Outline each blood parasite and name the species.
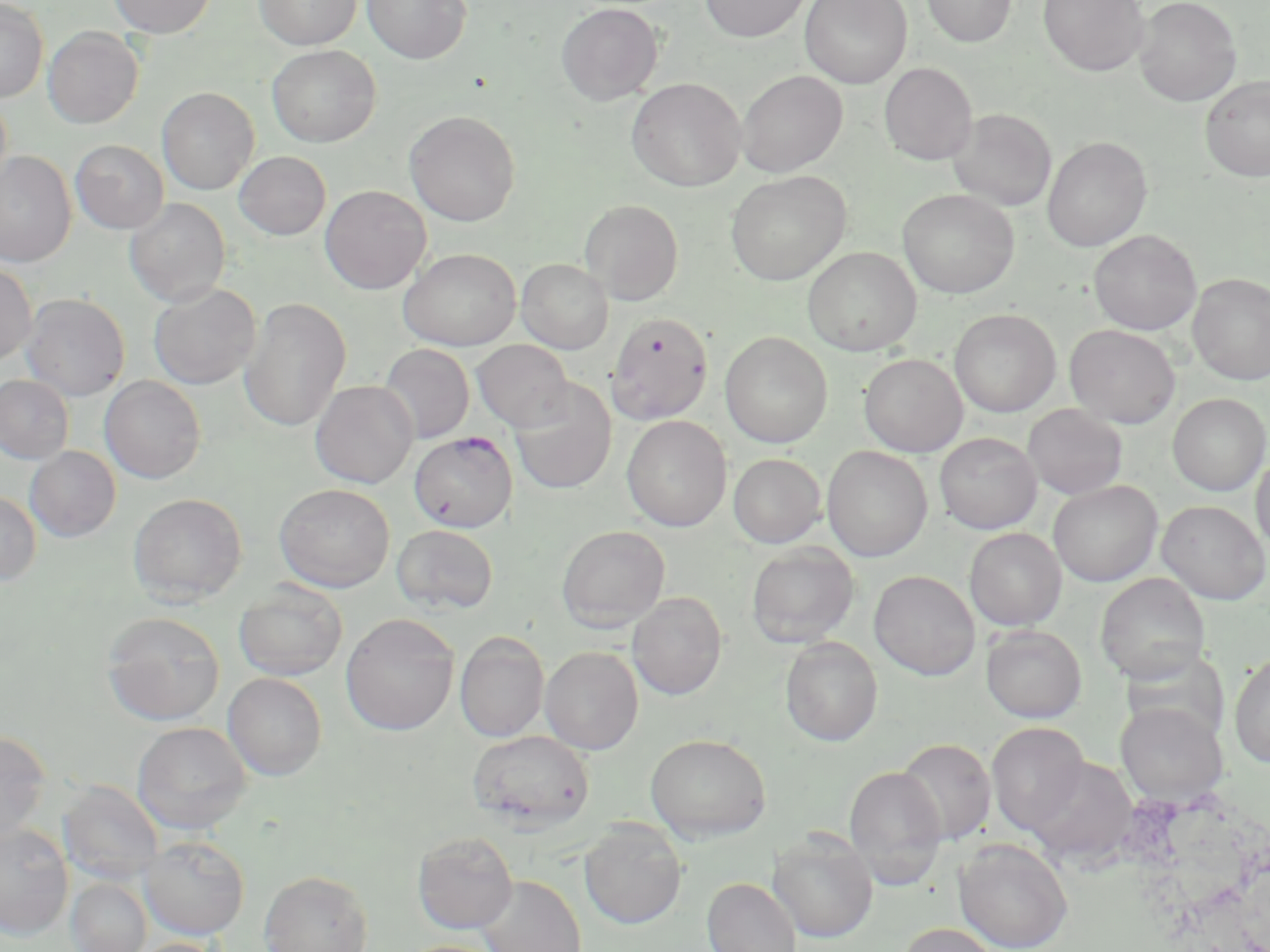

Approximate bounding boxes as named x1/y1/x2/y2 corners in pixels.
Plasmodium falciparum-infected red blood cells: (x1=409, y1=431, x2=518, y2=532).
No Plasmodium ovale, Plasmodium malariae, Plasmodium vivax, Babesia divergens, or Trypanosoma brucei observed.

{
  "slide_level_diagnosis": "Plasmodium falciparum",
  "modality": "light microscopy",
  "image_size": "1270×952 pixels",
  "stain": "May-Grünwald-Giemsa",
  "field_of_view": "single",
  "uninfected_red_blood_cell_locations": "approximate bounding boxes as named x1/y1/x2/y2 corners in pixels: (x1=109, y1=0, x2=216, y2=37), (x1=254, y1=0, x2=361, y2=50), (x1=363, y1=0, x2=471, y2=64), (x1=699, y1=0, x2=812, y2=42), (x1=800, y1=0, x2=911, y2=88), (x1=921, y1=0, x2=1016, y2=47), (x1=1038, y1=0, x2=1149, y2=77), (x1=1134, y1=0, x2=1242, y2=106), (x1=0, y1=1, x2=48, y2=102), (x1=555, y1=2, x2=663, y2=105), (x1=43, y1=26, x2=143, y2=128), (x1=267, y1=45, x2=381, y2=147), (x1=879, y1=62, x2=978, y2=165), (x1=737, y1=70, x2=848, y2=177), (x1=1200, y1=75, x2=1270, y2=182), (x1=626, y1=77, x2=746, y2=192), (x1=157, y1=87, x2=259, y2=195), (x1=0, y1=92, x2=12, y2=199), (x1=948, y1=108, x2=1056, y2=212), (x1=405, y1=110, x2=521, y2=226), (x1=1042, y1=136, x2=1152, y2=252), (x1=70, y1=139, x2=169, y2=234), (x1=0, y1=151, x2=76, y2=268), (x1=234, y1=151, x2=331, y2=240), (x1=726, y1=170, x2=850, y2=285), (x1=320, y1=185, x2=431, y2=294), (x1=898, y1=189, x2=1019, y2=298), (x1=125, y1=198, x2=231, y2=306), (x1=579, y1=199, x2=684, y2=304), (x1=1089, y1=229, x2=1201, y2=335), (x1=803, y1=246, x2=921, y2=355), (x1=398, y1=247, x2=521, y2=351), (x1=517, y1=259, x2=612, y2=354), (x1=0, y1=261, x2=37, y2=366), (x1=1188, y1=273, x2=1270, y2=385), (x1=149, y1=283, x2=261, y2=389), (x1=21, y1=293, x2=130, y2=401), (x1=239, y1=297, x2=352, y2=433), (x1=949, y1=309, x2=1061, y2=417), (x1=607, y1=312, x2=713, y2=424), (x1=1064, y1=325, x2=1180, y2=428), (x1=720, y1=332, x2=832, y2=448), (x1=472, y1=340, x2=573, y2=431), (x1=379, y1=343, x2=475, y2=443), (x1=859, y1=354, x2=968, y2=457), (x1=0, y1=375, x2=74, y2=464), (x1=100, y1=376, x2=206, y2=483), (x1=510, y1=379, x2=616, y2=494), (x1=310, y1=380, x2=418, y2=488), (x1=1167, y1=393, x2=1269, y2=496), (x1=1022, y1=404, x2=1128, y2=500), (x1=622, y1=415, x2=731, y2=532), (x1=934, y1=433, x2=1042, y2=533), (x1=24, y1=446, x2=121, y2=541), (x1=822, y1=446, x2=932, y2=562), (x1=1251, y1=450, x2=1270, y2=557), (x1=728, y1=453, x2=826, y2=548), (x1=1048, y1=480, x2=1162, y2=586), (x1=274, y1=483, x2=395, y2=591), (x1=0, y1=492, x2=42, y2=585), (x1=128, y1=492, x2=247, y2=604), (x1=1157, y1=500, x2=1269, y2=604), (x1=392, y1=524, x2=498, y2=615), (x1=556, y1=525, x2=670, y2=631), (x1=964, y1=528, x2=1066, y2=631), (x1=746, y1=543, x2=860, y2=648), (x1=869, y1=570, x2=980, y2=680), (x1=1095, y1=573, x2=1210, y2=684), (x1=233, y1=582, x2=348, y2=682), (x1=628, y1=591, x2=727, y2=700), (x1=101, y1=611, x2=226, y2=726), (x1=340, y1=613, x2=459, y2=736), (x1=981, y1=625, x2=1087, y2=722), (x1=455, y1=631, x2=549, y2=742), (x1=780, y1=636, x2=883, y2=746), (x1=540, y1=646, x2=643, y2=754), (x1=1229, y1=653, x2=1270, y2=768), (x1=223, y1=672, x2=328, y2=780), (x1=1115, y1=702, x2=1228, y2=804), (x1=132, y1=721, x2=251, y2=834), (x1=986, y1=722, x2=1089, y2=835), (x1=467, y1=729, x2=595, y2=830), (x1=0, y1=731, x2=50, y2=843), (x1=645, y1=733, x2=771, y2=842), (x1=897, y1=738, x2=996, y2=845), (x1=1026, y1=757, x2=1138, y2=866), (x1=844, y1=765, x2=947, y2=886), (x1=57, y1=781, x2=164, y2=885), (x1=579, y1=820, x2=687, y2=929), (x1=0, y1=823, x2=73, y2=939), (x1=773, y1=829, x2=878, y2=943), (x1=412, y1=831, x2=518, y2=934), (x1=139, y1=835, x2=250, y2=939), (x1=954, y1=838, x2=1073, y2=952), (x1=258, y1=870, x2=374, y2=952), (x1=477, y1=874, x2=586, y2=952), (x1=702, y1=877, x2=799, y2=952), (x1=66, y1=878, x2=152, y2=952), (x1=897, y1=922, x2=1001, y2=952), (x1=123, y1=937, x2=231, y2=952), (x1=399, y1=939, x2=504, y2=952)",
  "magnification": "1000x",
  "preparation": "thin blood smear"
}